Assess the morphology of the erythrocytes.
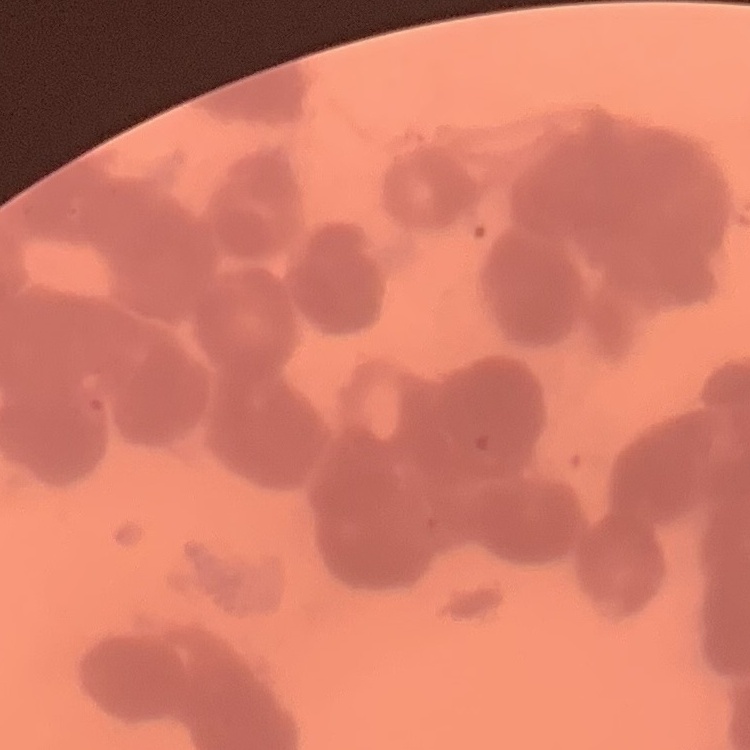

They show rouleaux formation.

Summary:
  - Image type: one tile cut from a larger photomicrograph
  - Preparation: thin blood smear
  - Stain: Field's or Giemsa